Mark where platelets are.
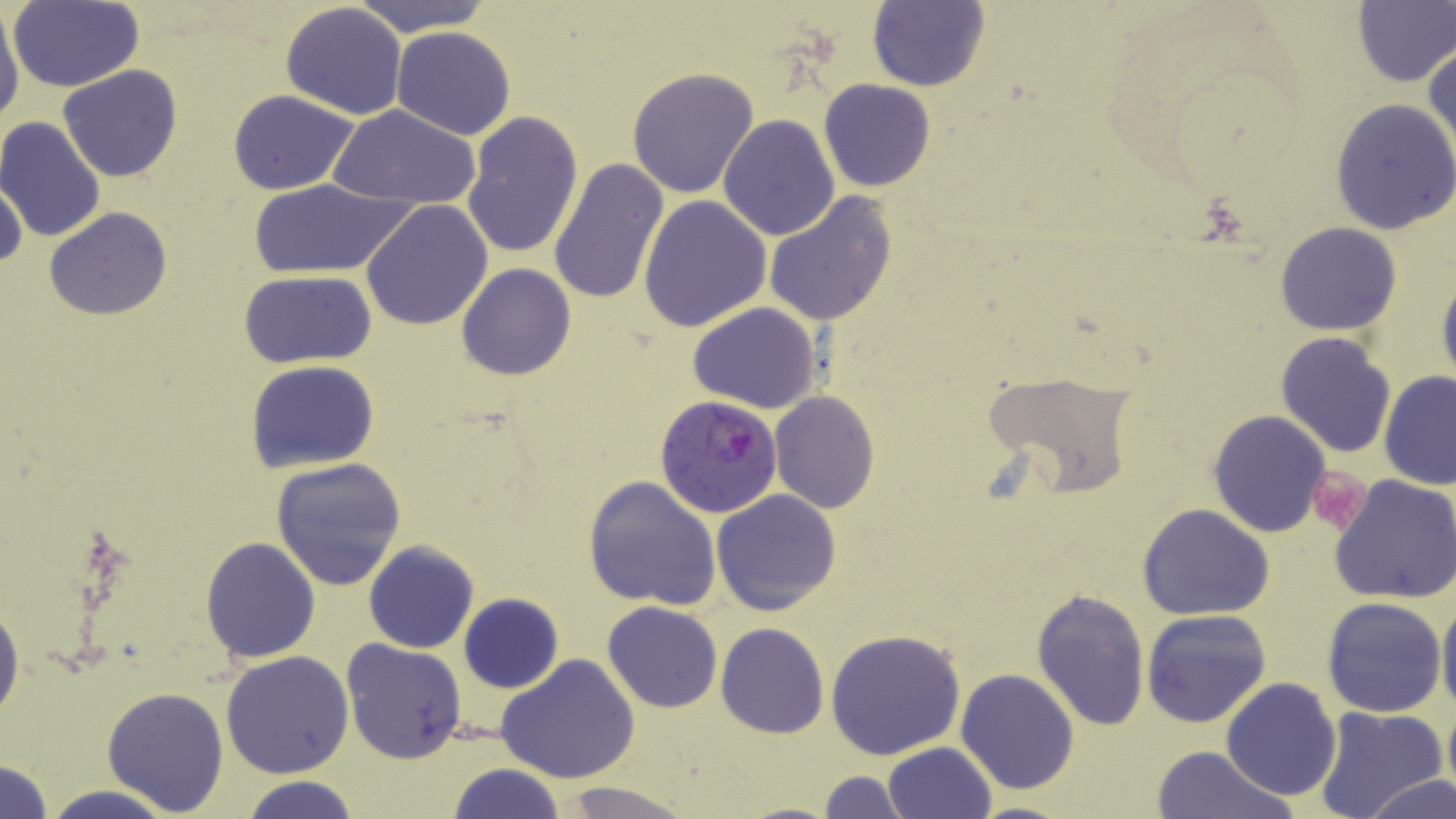
Approximate bounding boxes as (x1,y1)-(x2,y2) corner pairs in pixels.
Platelets: (1306,465)-(1371,537).

Uninfected red blood cell locations: (349,0)-(496,35), (8,1)-(145,91), (282,2)-(407,120), (866,2)-(990,90), (1353,3)-(1456,86), (0,5)-(24,129), (391,26)-(516,139), (1425,43)-(1456,166), (57,65)-(183,183), (626,67)-(760,197), (819,79)-(935,192), (228,89)-(359,195), (1329,99)-(1456,235), (329,104)-(482,209), (460,109)-(585,261), (717,114)-(840,241), (0,116)-(106,243), (549,157)-(670,307), (0,177)-(27,275), (248,178)-(410,279), (639,194)-(772,333), (762,194)-(899,326), (360,201)-(493,331), (42,208)-(172,319), (1275,221)-(1402,335), (457,264)-(576,380), (1436,268)-(1456,390), (239,270)-(376,369), (687,302)-(820,415), (1275,332)-(1398,458), (246,360)-(380,472), (1378,370)-(1456,489), (986,371)-(1139,495), (769,391)-(881,512), (1207,409)-(1332,538), (269,457)-(407,590), (583,474)-(723,611), (1328,474)-(1456,606), (711,486)-(843,617), (1136,503)-(1277,620), (200,535)-(321,663), (364,541)-(480,653), (1030,587)-(1150,732), (1437,591)-(1456,719), (459,593)-(563,692), (0,595)-(23,727), (1320,596)-(1447,718), (603,601)-(723,713), (1141,609)-(1272,728), (716,622)-(827,737), (825,629)-(968,759), (341,638)-(467,764), (219,650)-(354,778), (496,654)-(640,784), (955,668)-(1081,795), (1221,678)-(1342,801), (103,686)-(231,814), (1441,699)-(1456,806), (1313,705)-(1448,819), (883,741)-(997,819), (1151,745)-(1295,819), (0,758)-(53,819), (448,763)-(564,819), (818,770)-(907,819), (241,775)-(362,819), (1365,775)-(1455,819), (555,781)-(698,819), (40,784)-(180,819), (965,800)-(1082,819), (733,801)-(845,818). Plasmodium falciparum-infected red blood cell locations: (654,395)-(784,518). Slide-level diagnosis: Plasmodium falciparum. One field of a larger specimen. Image is 1456×819 pixels. 1000x magnification. Thin blood smear. May-Grünwald-Giemsa stain. Optical microscopy.